Assess this cell for malaria.
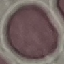
It is uninfected.

image type = cell patch, automatically extracted from a larger field of view and resized to 64 × 64 pixels
capture = smartphone camera at the microscope eyepiece
preparation = thin smear
stain = Giemsa